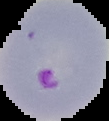
Image is 109×121 pixels. From a thin blood film. Result: Plasmodium parasites identified. Segmented cell region on a black background.